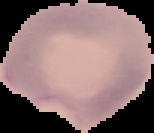 Image is 154×133 pixels. From a thin blood film. Cell region segmented out of the field of view; the surrounding area is masked to black. Result: malaria parasites detected.